Comment on the morphology of the red blood cells.
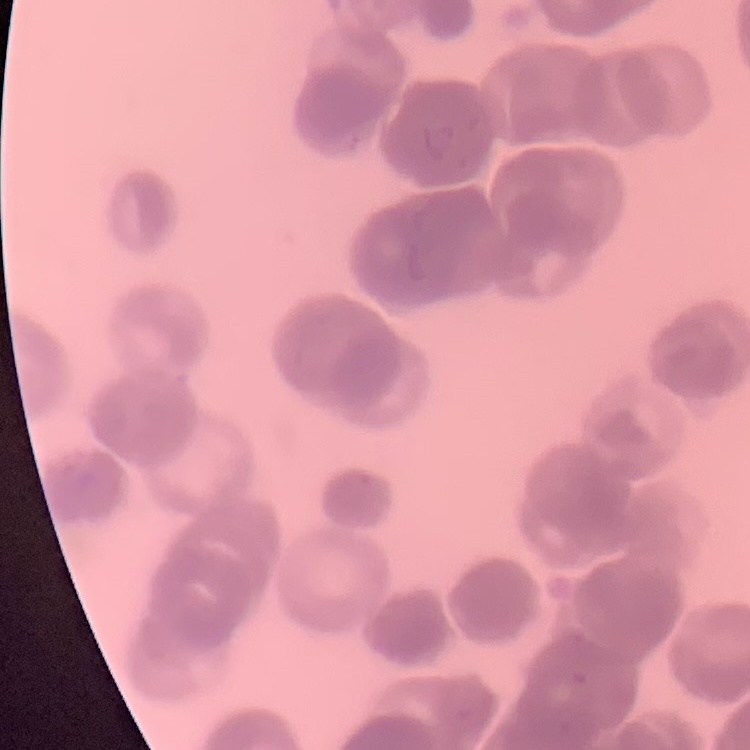

They show rouleaux formation.

image type = square crop of a larger photomicrograph
stain = Field's or Giemsa
preparation = thin blood film